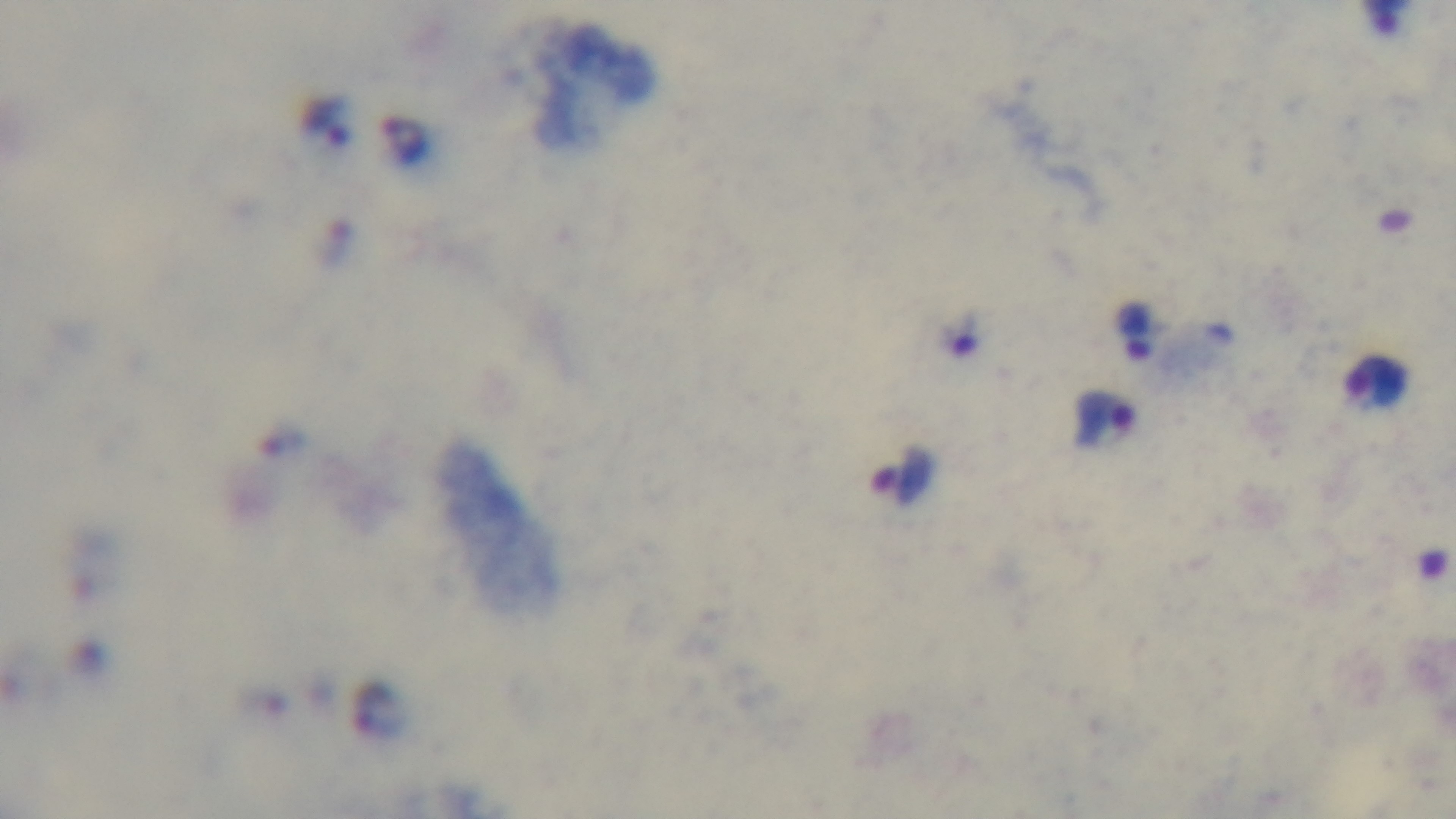
Single field of view. Preparation: thick blood film. Oil-immersion objective, 100x. Giemsa-stained. Malaria status: positive. Light microscopy. Captured with a mounted 4K digital camera.